Evaluate for malaria.
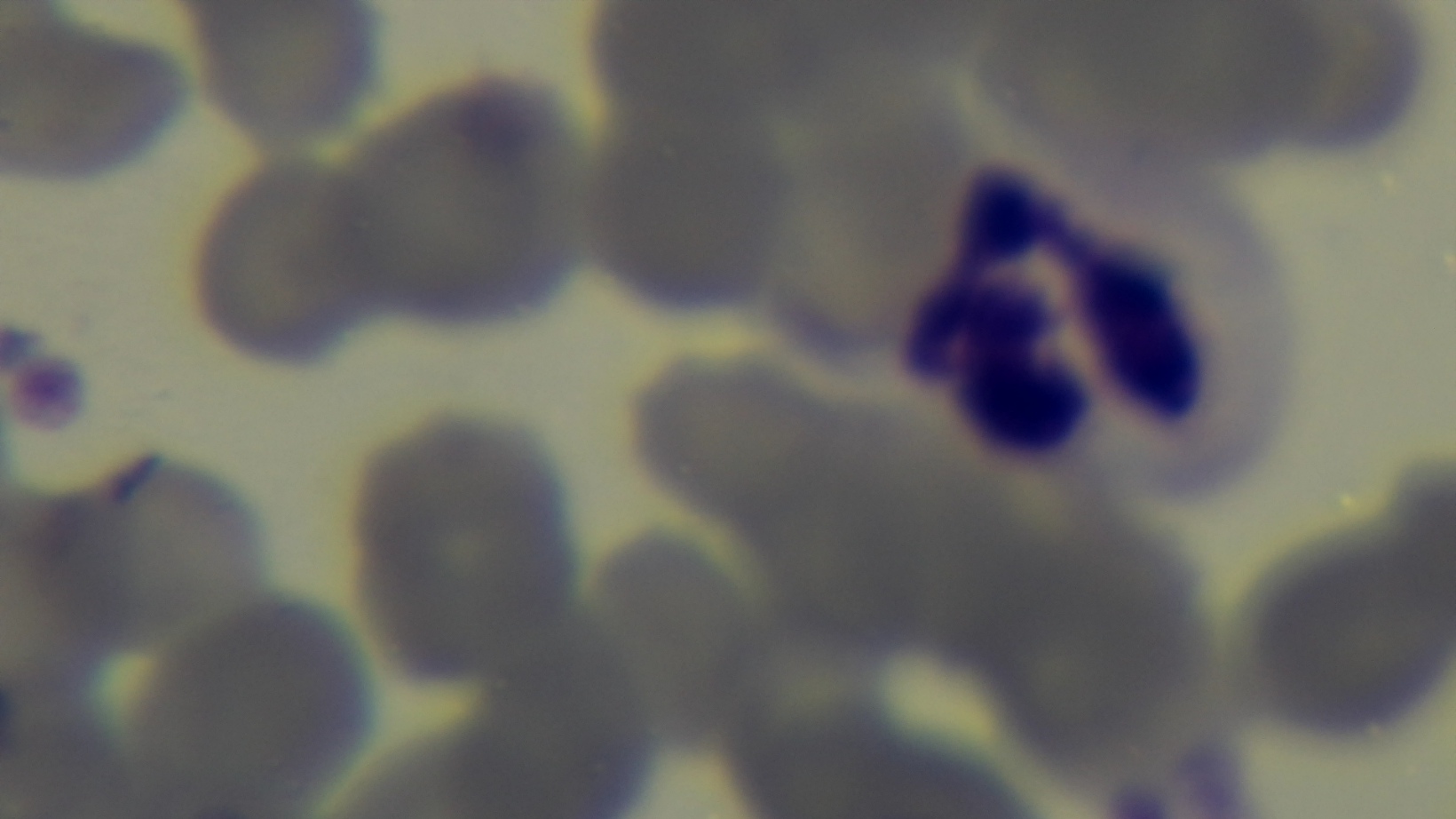

It is uninfected.

Summary:
  - Stain: Giemsa
  - Field of view: one from the slide
  - Objective: 100x oil immersion
  - Capture: mounted 4K digital camera
  - Modality: light microscopy
  - Preparation: thin blood film